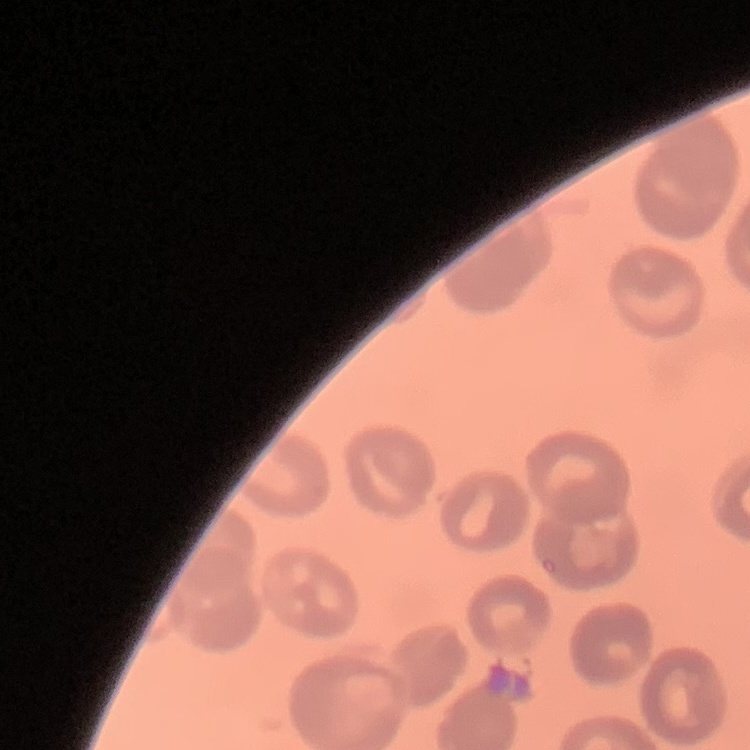

{
  "red_blood_cell_morphology": "no rouleaux formation",
  "stain": "Field's or Giemsa",
  "image_type": "square crop of a larger photomicrograph",
  "preparation": "thin peripheral smear"
}